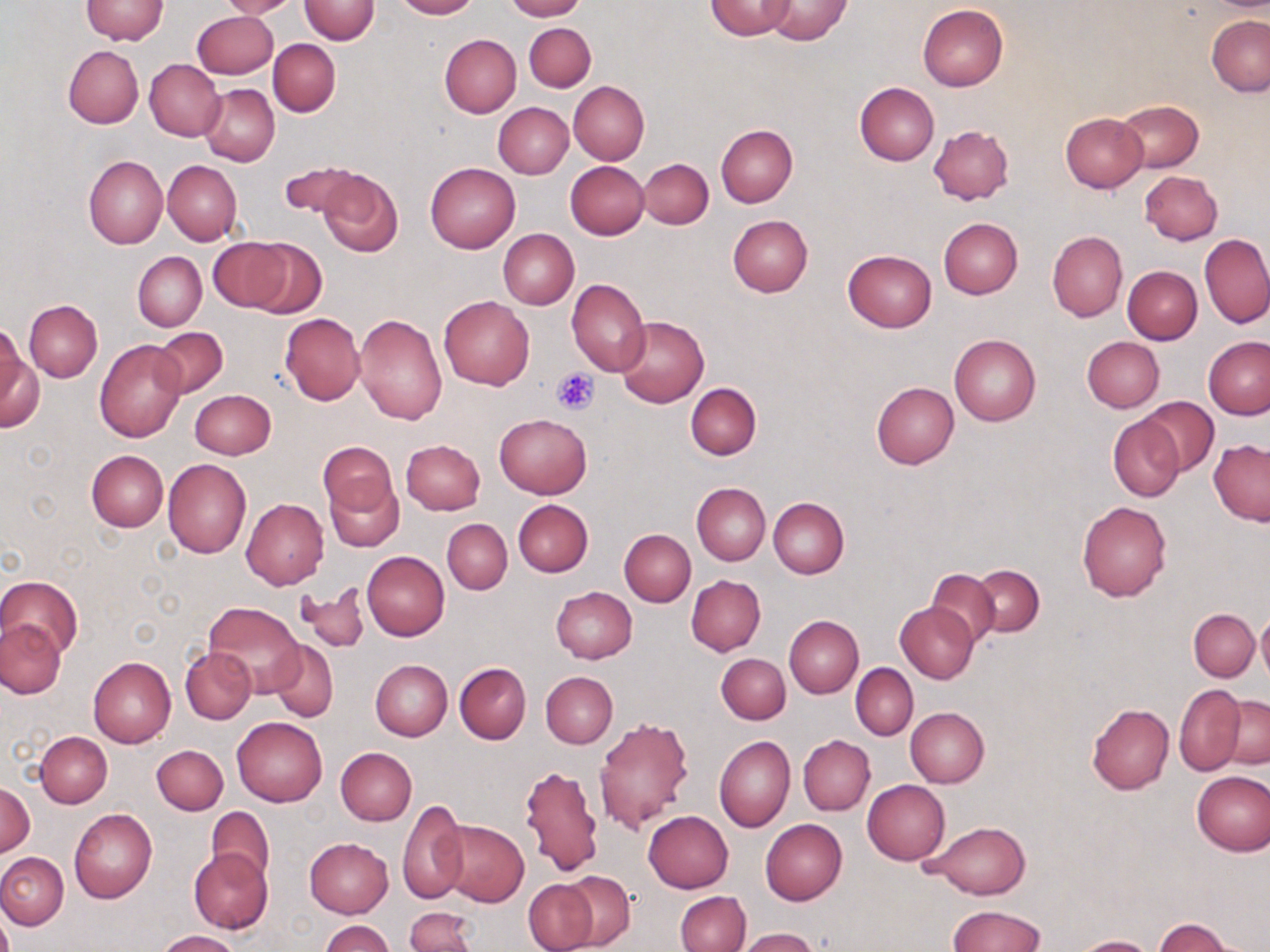
Summary:
  - Coordinate format: approximate bounding boxes as (x1, y1, x2, y2) in pixels
  - Uninfected red blood cell locations: (81, 0, 168, 44), (219, 0, 299, 19), (299, 0, 379, 44), (391, 0, 480, 19), (503, 0, 584, 21), (706, 0, 796, 39), (762, 0, 850, 44), (918, 4, 1008, 92), (192, 11, 278, 79), (1207, 15, 1270, 96), (523, 22, 596, 92), (440, 34, 520, 117), (268, 38, 341, 116), (63, 45, 143, 128), (145, 59, 224, 141), (568, 81, 649, 164), (854, 82, 939, 165), (200, 84, 279, 166), (1117, 100, 1203, 172), (494, 102, 573, 178), (1059, 113, 1148, 192), (716, 123, 798, 208), (929, 125, 1015, 204), (83, 155, 167, 249), (639, 158, 713, 228), (162, 160, 242, 245), (280, 160, 361, 221), (565, 161, 649, 239), (425, 162, 519, 252), (315, 167, 404, 258), (1139, 170, 1221, 245), (728, 215, 812, 298), (939, 217, 1022, 298), (498, 228, 579, 309), (1047, 230, 1127, 321), (1200, 233, 1269, 329), (242, 238, 326, 319), (208, 239, 293, 311), (843, 249, 936, 332), (132, 251, 206, 331), (1122, 266, 1202, 344), (567, 279, 650, 376), (438, 296, 534, 390), (24, 300, 102, 382), (280, 313, 365, 405), (355, 313, 448, 426), (615, 315, 709, 408), (0, 322, 29, 414), (152, 327, 227, 397), (949, 335, 1041, 425), (1203, 336, 1270, 419), (1081, 337, 1164, 413), (95, 341, 187, 442), (1, 348, 44, 432), (871, 381, 959, 468), (686, 382, 762, 460), (190, 389, 276, 459), (1137, 397, 1219, 476), (495, 413, 592, 498), (1108, 414, 1185, 501), (1209, 439, 1270, 525), (401, 440, 485, 514), (319, 441, 396, 515), (86, 450, 168, 532), (163, 458, 251, 557), (325, 478, 403, 551), (692, 482, 770, 565), (768, 497, 849, 578), (241, 498, 329, 589), (513, 499, 592, 576), (1077, 501, 1172, 601), (442, 519, 511, 594), (619, 529, 695, 606), (361, 551, 450, 640), (971, 564, 1044, 636), (925, 567, 1001, 647), (687, 575, 765, 655), (0, 576, 81, 660), (298, 582, 370, 653), (549, 586, 636, 663), (203, 601, 305, 696), (895, 602, 979, 683), (1189, 609, 1260, 683), (1256, 611, 1270, 684), (784, 616, 863, 697), (1, 618, 65, 699), (269, 640, 339, 722), (180, 647, 256, 724), (716, 653, 790, 724), (88, 655, 175, 748), (370, 660, 452, 741), (454, 662, 531, 743), (851, 664, 917, 740), (541, 671, 617, 748), (1174, 685, 1244, 776), (1221, 695, 1270, 769), (1086, 703, 1173, 795), (906, 708, 989, 788), (594, 715, 695, 834), (232, 717, 327, 807), (36, 731, 112, 807), (714, 734, 795, 832), (798, 734, 875, 815), (153, 745, 227, 815), (335, 748, 417, 826), (519, 763, 603, 876), (1191, 771, 1269, 856), (863, 780, 950, 864), (1, 783, 35, 856), (398, 800, 467, 905), (206, 805, 275, 884), (69, 808, 157, 903), (643, 811, 733, 892), (436, 819, 529, 907), (760, 819, 848, 905), (925, 821, 1031, 899), (305, 838, 394, 918), (189, 849, 273, 934), (0, 852, 68, 929), (558, 871, 636, 950), (521, 878, 599, 952), (676, 891, 750, 952), (947, 905, 1045, 951), (405, 907, 477, 952), (1152, 918, 1239, 951), (322, 919, 392, 952), (738, 928, 821, 952), (155, 930, 242, 952), (1072, 936, 1156, 952)
  - Platelet locations: (551, 366, 599, 415)
  - Slide-level diagnosis: no evidence of blood parasites
  - Modality: optical microscopy
  - Image size: 1270×952 pixels
  - Stain: May-Grünwald-Giemsa
  - Magnification: 1000x
  - Preparation: thin blood film
  - Field of view: one of a larger specimen